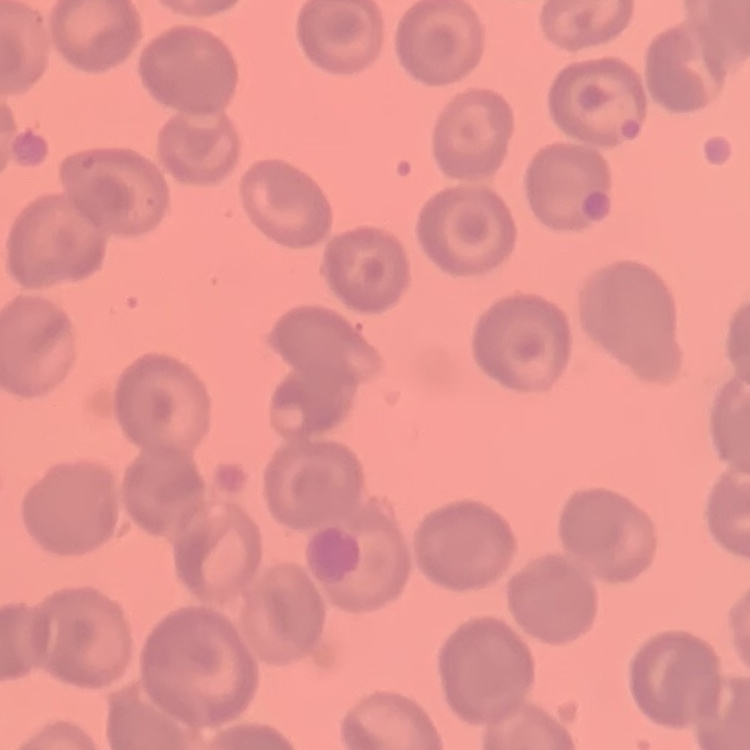
erythrocyte morphology = no rouleaux formation
preparation = thin peripheral smear
stain = Field's or Giemsa
image type = one tile cut from a larger photomicrograph